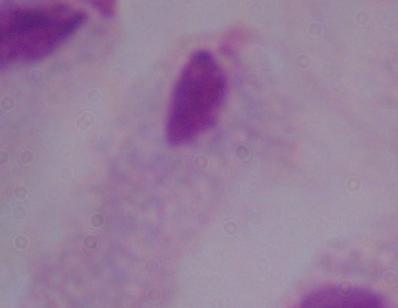
Captured at 1000x magnification. Photomicrograph. A trichomonad is seen.